Locate every malaria parasite.
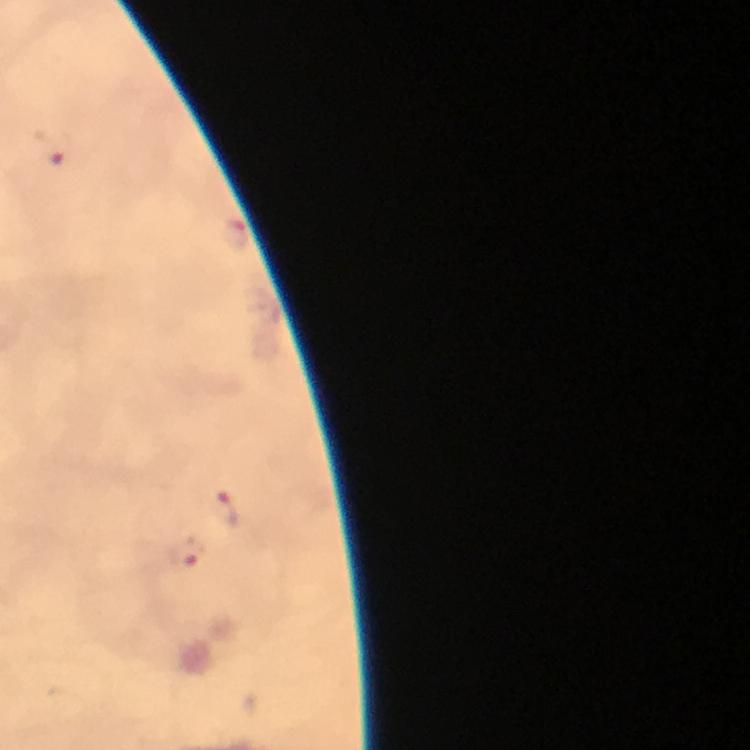

Approximate centers as (x, y) in pixels.
Malaria parasites: (50, 150), (235, 236), (227, 513), (186, 551).

context: from a malaria diagnostic workup
immersion_oil: used
capture: smartphone mounted on the microscope
stain: Giemsa
preparation: thick blood smear
cropped_from: one field of view
image_size: 750×750 pixels
magnification: 100x